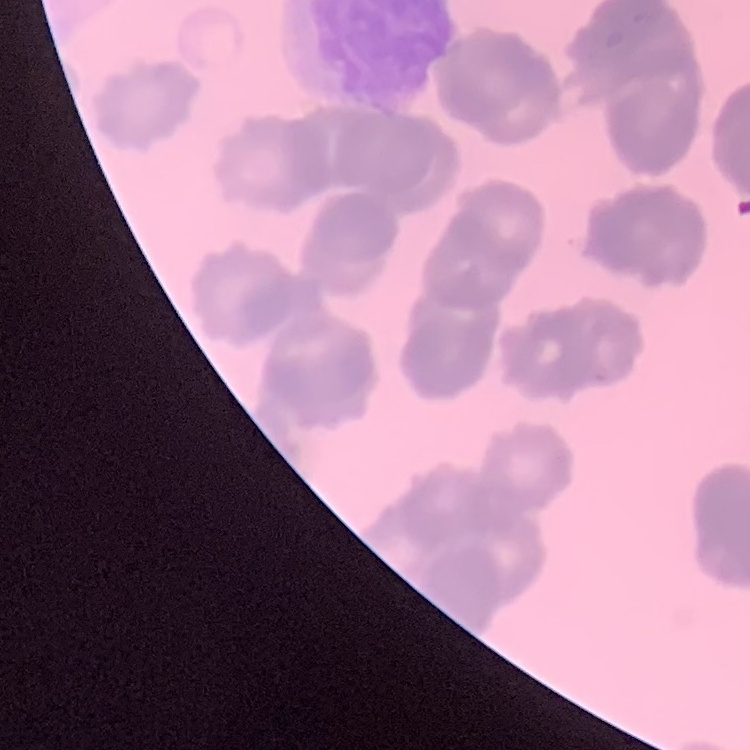

Summary:
  - Red blood cell morphology: rouleaux formation
  - Image type: square crop of a larger photomicrograph
  - Preparation: thin blood smear
  - Stain: Field's or Giemsa